Outline each Plasmodium falciparum-infected red blood cell.
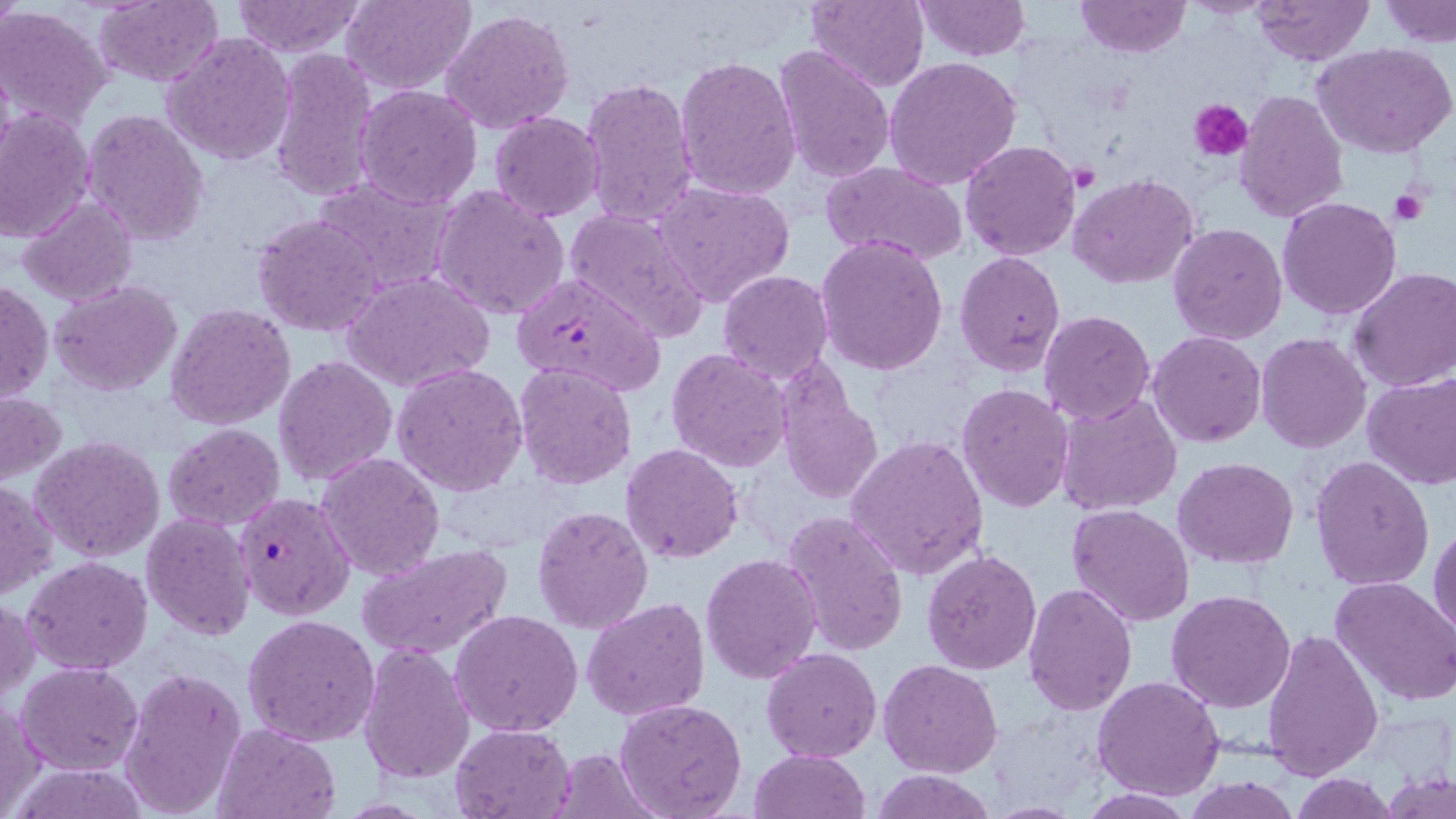
Approximate bounding boxes as (x1, y1, x2, y2) in pixels.
Plasmodium falciparum-infected red blood cells: (510, 269, 667, 399), (234, 491, 356, 620).

slide_level_diagnosis: Plasmodium falciparum
field_of_view: single
uninfected_red_blood_cell_locations: 'approximate bounding boxes as (x1, y1, x2, y2) in pixels: (93, 0, 223, 88), (342, 0, 477, 94), (804, 0, 930, 93), (915, 0, 1032, 62), (1077, 0, 1190, 57), (1251, 0, 1373, 66), (1382, 0, 1456, 46), (229, 1, 370, 58), (1, 5, 113, 130), (442, 7, 575, 136), (162, 31, 296, 165), (772, 43, 894, 184), (1313, 43, 1455, 158), (267, 46, 381, 203), (675, 55, 801, 198), (884, 58, 1024, 189), (580, 76, 699, 227), (355, 84, 483, 210), (1235, 90, 1349, 223), (0, 106, 97, 246), (84, 109, 212, 247), (490, 112, 604, 221), (960, 139, 1082, 260), (823, 161, 968, 266), (1068, 173, 1201, 291), (311, 176, 456, 293), (652, 182, 794, 306), (431, 183, 571, 321), (1277, 196, 1402, 320), (19, 197, 138, 306), (564, 208, 711, 343), (253, 213, 384, 336), (1168, 223, 1289, 346), (816, 235, 949, 376), (955, 251, 1066, 374), (1349, 268, 1456, 392), (718, 270, 833, 384), (344, 271, 496, 393), (1, 280, 52, 406), (50, 280, 184, 398), (164, 302, 295, 430), (1039, 310, 1155, 425), (1149, 332, 1266, 447), (1256, 333, 1371, 454), (667, 348, 793, 472), (274, 355, 397, 484), (514, 361, 638, 488), (777, 362, 884, 507), (392, 364, 530, 496), (1362, 374, 1456, 492), (955, 384, 1075, 513), (0, 391, 67, 484), (1056, 392, 1183, 515), (164, 423, 286, 530), (847, 434, 989, 579), (32, 435, 166, 563), (621, 444, 745, 564), (317, 453, 444, 581), (1310, 456, 1436, 591), (1173, 458, 1298, 569), (1, 478, 57, 600), (1068, 504, 1195, 627), (532, 505, 653, 633), (783, 509, 908, 655), (140, 513, 255, 642), (1429, 522, 1456, 639), (356, 542, 515, 662), (921, 549, 1042, 674), (700, 552, 821, 686), (24, 557, 151, 675), (1331, 576, 1456, 708), (1022, 584, 1139, 716), (1166, 590, 1298, 712), (1, 597, 37, 706), (583, 597, 710, 721), (451, 609, 584, 737), (243, 614, 381, 747), (1262, 627, 1383, 780), (357, 640, 475, 784), (762, 648, 884, 763), (877, 659, 1003, 778), (15, 661, 143, 776), (119, 666, 247, 818), (1092, 676, 1224, 801), (614, 699, 748, 819), (0, 701, 45, 817), (450, 722, 577, 819), (212, 723, 339, 819), (550, 747, 660, 817), (750, 748, 870, 818), (7, 762, 153, 819), (869, 767, 996, 819), (1382, 771, 1456, 819), (1288, 774, 1400, 818), (1185, 777, 1301, 818), (1080, 788, 1197, 818)'
modality: optical microscopy
magnification: 1000x
image_size: 1456×819 pixels
stain: May-Grünwald-Giemsa
platelet_locations: 'approximate bounding boxes as (x1, y1, x2, y2) in pixels: (1191, 99, 1253, 161), (1388, 186, 1424, 225)'
preparation: thin blood film